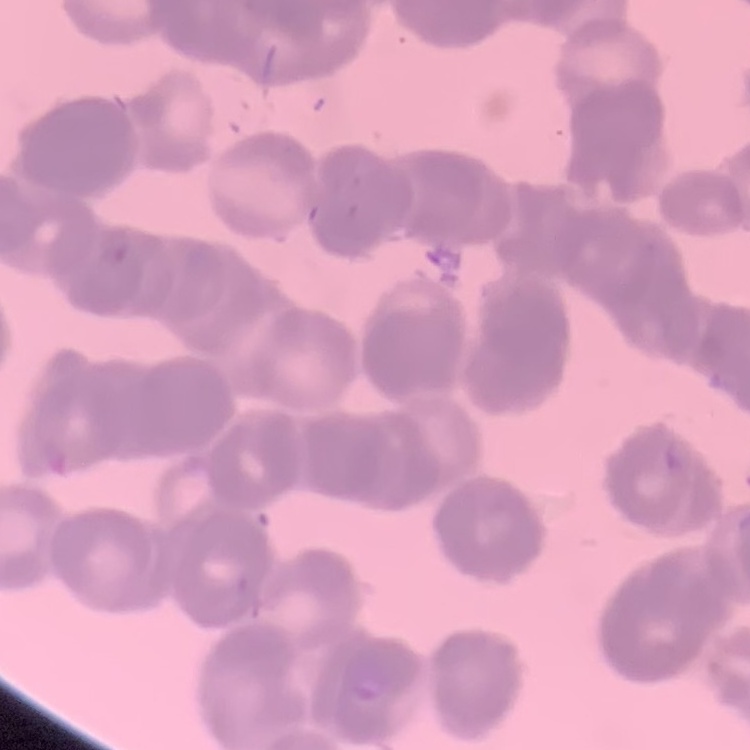 The erythrocytes show rouleaux formation. Square crop of a larger photomicrograph. Stained with either Field's or Giemsa. Thin blood film.